Give the extent of all uninfected red blood cells.
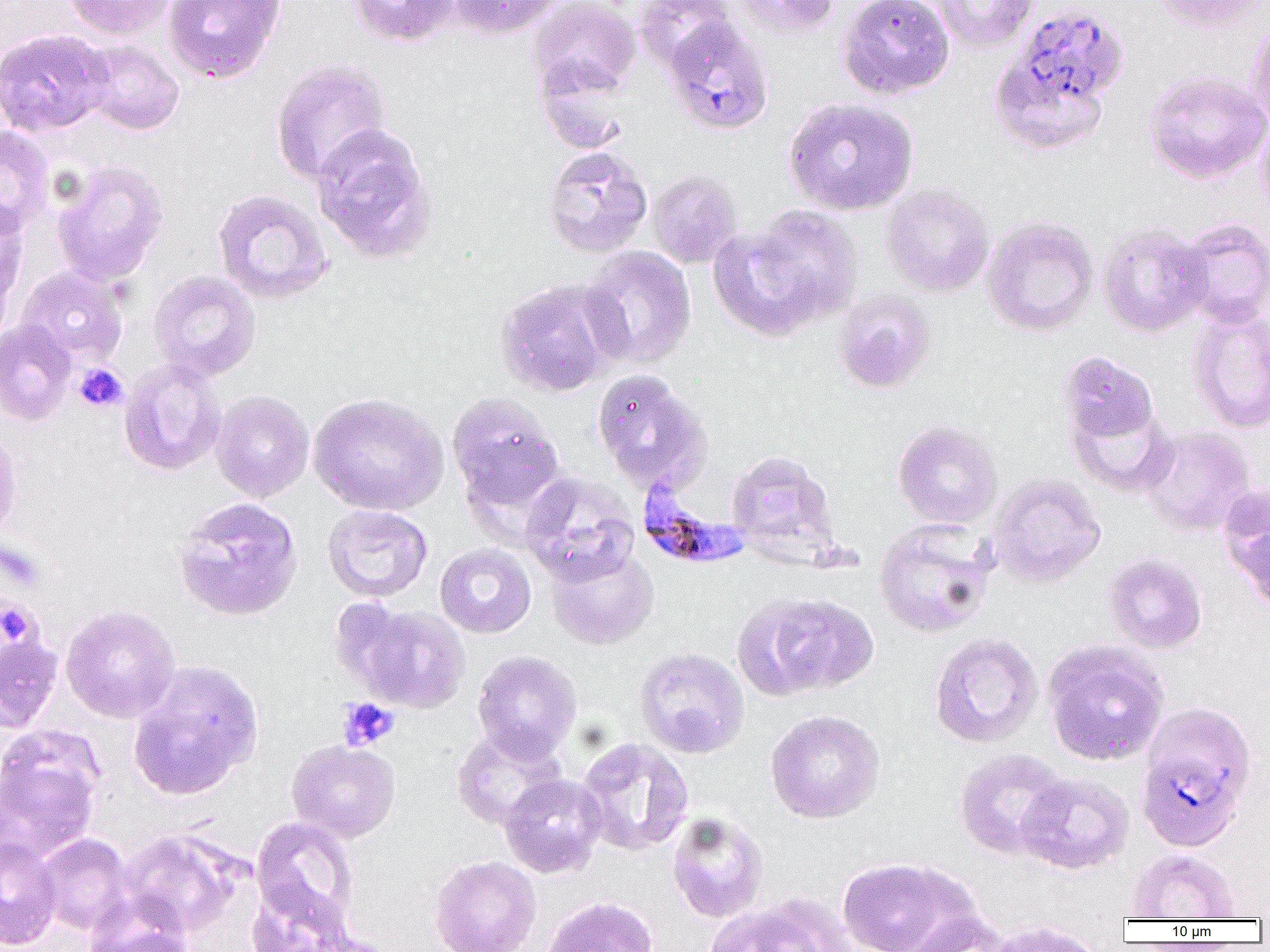
Approximate bounding boxes as (x1,y1)-(x2,y2) corner pairs in pixels.
Uninfected red blood cells: (63,0)-(175,40), (161,0)-(286,83), (348,0)-(459,47), (447,0)-(565,39), (527,0)-(641,98), (633,0)-(738,72), (731,0)-(841,38), (837,0)-(956,99), (925,0)-(1039,52), (1150,0)-(1269,32), (1016,5)-(1129,108), (1247,17)-(1270,130), (663,18)-(774,135), (0,28)-(113,137), (80,39)-(184,135), (989,54)-(1108,156), (535,56)-(634,154), (270,59)-(391,186), (1144,70)-(1270,184), (783,97)-(919,216), (1256,117)-(1270,218), (310,123)-(437,264), (0,125)-(54,237), (542,146)-(653,258), (51,159)-(169,287), (646,170)-(743,268), (880,184)-(994,297), (212,189)-(333,305), (0,201)-(28,326), (736,204)-(864,333), (981,216)-(1099,337), (1177,218)-(1270,329), (1098,222)-(1212,337), (580,246)-(697,369), (16,267)-(128,369), (149,270)-(261,382), (494,279)-(618,398), (833,290)-(936,394), (1187,306)-(1270,434), (0,319)-(76,426), (1058,350)-(1159,446), (119,358)-(226,476), (591,368)-(711,494), (209,390)-(314,502), (308,392)-(449,516), (446,392)-(565,516), (1067,401)-(1179,498), (892,420)-(1003,529), (1140,424)-(1257,537), (0,426)-(22,544), (725,449)-(844,568), (519,472)-(639,587), (987,473)-(1107,589), (1221,489)-(1270,610), (173,497)-(303,622), (322,504)-(432,602), (873,518)-(996,638), (434,543)-(537,639), (546,546)-(659,650), (1102,552)-(1208,654), (738,592)-(878,699), (342,602)-(472,714), (60,604)-(180,723), (0,632)-(63,732), (928,632)-(1044,748), (1042,640)-(1169,766), (634,647)-(750,759), (471,650)-(582,762), (127,661)-(263,800), (1141,700)-(1257,789), (764,710)-(885,823), (451,726)-(567,830), (0,727)-(104,860), (575,737)-(695,856), (287,740)-(400,842), (954,748)-(1070,860), (1015,772)-(1135,874), (498,773)-(607,878), (667,811)-(769,922), (250,817)-(360,932), (117,829)-(246,937), (36,833)-(134,935), (0,836)-(62,949), (1127,849)-(1241,921), (429,855)-(541,952), (837,856)-(980,952), (245,883)-(359,952), (83,894)-(195,952), (540,896)-(660,952), (705,900)-(833,952), (900,912)-(1011,952), (981,920)-(1105,952).

Plasmodium falciparum-infected red blood cell locations: (636,474)-(751,569), (1143,753)-(1242,849). Platelet locations: (74,363)-(128,412), (0,601)-(37,645), (338,698)-(399,751). Slide-level diagnosis: Plasmodium falciparum. Light microscopy. Thin blood film. Image is 1270×952 pixels. 1000x magnification. Single field of view.